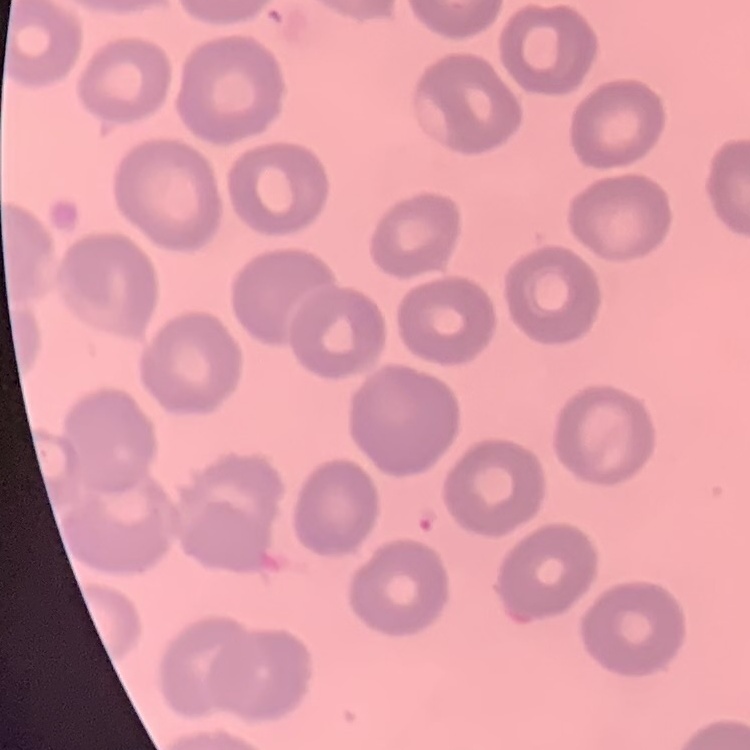

erythrocyte_morphology: no rouleaux formation
stain: Field's or Giemsa
preparation: thin blood smear
image_type: one tile cut from a larger photomicrograph